Report the malaria status of this cell.
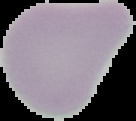
Uninfected.

preparation: thin blood smear
image_type: segmented cell region with the area outside set to black
image_size: 136×121 pixels